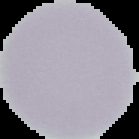

Summary:
  - Preparation: thin blood film
  - Malaria status: uninfected
  - Image size: 139×139 pixels
  - Image type: segmented cell region on a black background